Assess this cell for malaria.
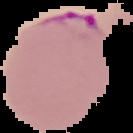
It is parasitized.

preparation = thin blood smear
image type = segmented cell region on a black background
image size = 133×133 pixels